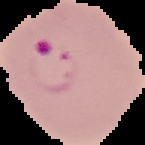 Segmented cell region on a black background. From a thin blood film. Image is 145×145 pixels. Malaria status: parasitized.